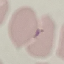

result = no malaria parasites seen
preparation = thin smear
stain = Giemsa
image type = cell patch, automatically extracted from a larger field of view and resized to 64 × 64 pixels
capture = smartphone through the microscope eyepiece